Identify the parasite.
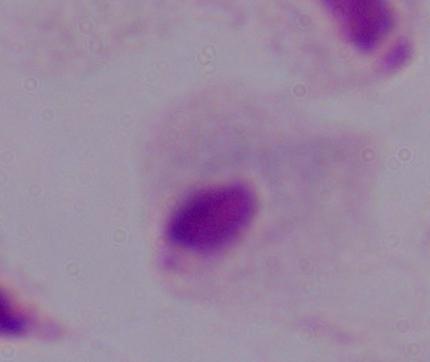
A trichomonad.

Summary:
  - Magnification: 1000x
  - Modality: photomicrograph